Identify the blood parasite species.
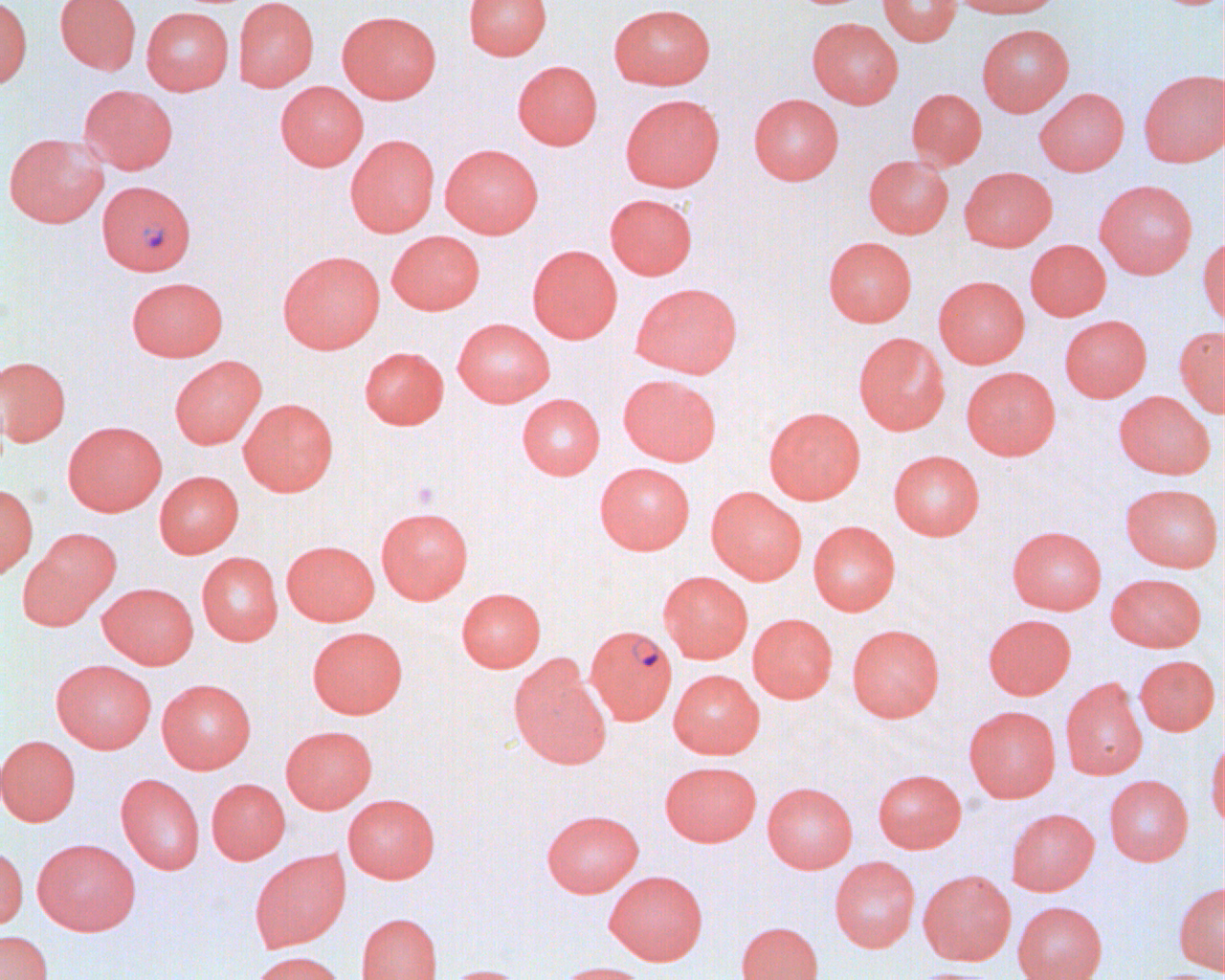

Plasmodium falciparum.

{
  "magnification": "1000x",
  "field_of_view": "single",
  "uninfected_red_blood_cell_locations": "approximate bounding boxes as (x1, y1, x2, y2) in pixels: (0, 0, 32, 89), (55, 0, 141, 74), (233, 0, 319, 91), (464, 0, 552, 60), (877, 0, 961, 46), (949, 0, 1063, 19), (55, 3, 233, 79), (609, 3, 716, 89), (141, 7, 234, 95), (337, 10, 441, 104), (807, 17, 903, 109), (976, 23, 1074, 116), (512, 60, 602, 150), (1138, 68, 1224, 167), (275, 81, 368, 170), (78, 84, 178, 174), (1034, 87, 1129, 176), (906, 88, 987, 170), (620, 93, 725, 191), (748, 94, 844, 184), (3, 133, 108, 227), (345, 134, 440, 236), (440, 144, 543, 238), (863, 155, 954, 238), (959, 166, 1057, 251), (1094, 180, 1197, 279), (604, 193, 697, 280), (387, 230, 485, 315), (1198, 235, 1225, 328), (824, 236, 917, 326), (1025, 239, 1111, 321), (527, 245, 622, 343), (278, 250, 385, 353), (126, 276, 228, 361), (933, 276, 1029, 368), (631, 282, 743, 378), (1059, 314, 1151, 402), (452, 318, 554, 407), (1174, 326, 1225, 417), (854, 332, 950, 434), (359, 346, 449, 429), (169, 355, 266, 449), (0, 356, 71, 446), (961, 366, 1061, 459), (618, 374, 722, 465), (1114, 391, 1215, 479), (517, 393, 605, 479), (238, 398, 338, 496), (763, 407, 865, 504), (62, 421, 167, 516), (888, 450, 985, 540), (594, 462, 695, 554), (154, 471, 244, 558), (0, 483, 38, 579), (1120, 483, 1224, 572), (706, 487, 807, 584), (376, 507, 474, 604), (808, 520, 900, 615), (1007, 525, 1107, 614), (19, 529, 121, 629), (281, 540, 379, 626), (195, 549, 378, 638), (196, 551, 283, 645), (658, 571, 753, 663), (1106, 573, 1206, 652), (97, 582, 199, 669), (456, 587, 545, 672), (747, 613, 838, 703), (983, 614, 1076, 699), (846, 624, 945, 722), (307, 626, 408, 719), (508, 654, 612, 770), (1134, 655, 1219, 735), (50, 659, 156, 753), (669, 669, 764, 758), (1060, 677, 1148, 780), (156, 678, 257, 773), (964, 705, 1061, 802), (281, 725, 377, 813), (0, 735, 81, 826), (1206, 737, 1225, 833), (659, 761, 761, 846), (873, 769, 966, 853), (116, 773, 205, 874), (1104, 775, 1194, 865), (206, 778, 290, 864), (762, 782, 858, 872), (342, 793, 440, 882), (1007, 808, 1099, 895), (541, 809, 644, 897), (32, 838, 141, 935), (0, 845, 28, 931), (250, 850, 351, 952), (829, 856, 920, 952), (918, 869, 1016, 965), (604, 870, 708, 964), (1173, 882, 1225, 974), (1012, 900, 1108, 980), (356, 912, 442, 980), (736, 921, 824, 980), (0, 930, 53, 980), (248, 951, 346, 980), (554, 961, 651, 980), (440, 965, 529, 980), (907, 967, 1005, 980)",
  "preparation": "thin blood film",
  "plasmodium_falciparum_infected_red_blood_cell_locations": "approximate bounding boxes as (x1, y1, x2, y2) in pixels: (97, 180, 196, 275), (589, 628, 680, 729)",
  "image_size": "1225×980 pixels",
  "modality": "optical microscopy"
}